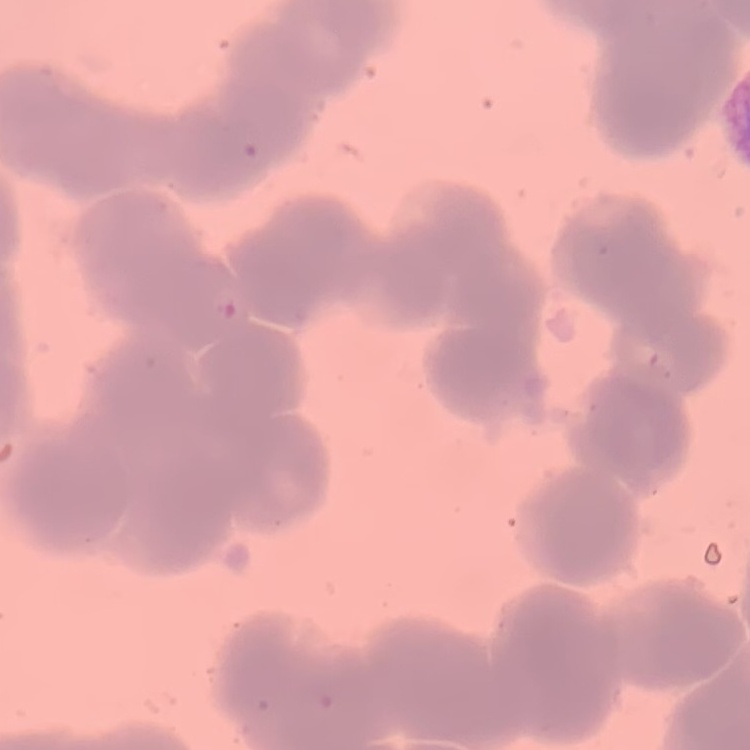 The erythrocytes show rouleaux formation. Field's or Giemsa stain. Square crop of a larger photomicrograph. Thin peripheral smear.